Outline each blood parasite and name the species.
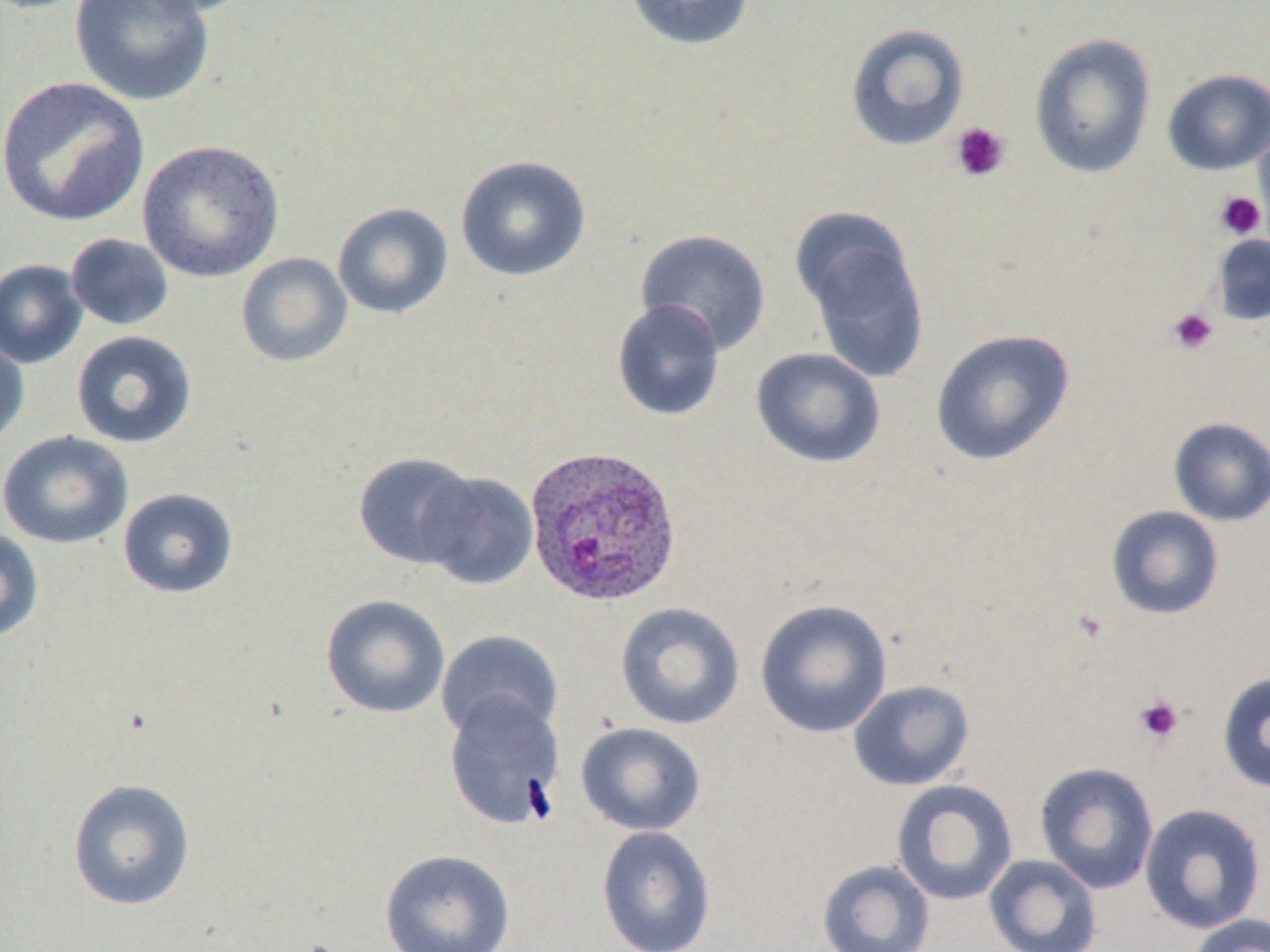
Approximate bounding boxes as (x1,y1)-(x2,y2) corner pairs in pixels.
Plasmodium ovale-infected red blood cells: (523,443)-(682,607).
No Plasmodium falciparum, Plasmodium malariae, Plasmodium vivax, Babesia divergens, or Trypanosoma brucei observed.

Summary:
  - Platelet locations: (950,122)-(1011,183), (1215,191)-(1265,239), (1167,308)-(1219,355), (1072,608)-(1107,645), (1134,695)-(1184,745)
  - Uninfected red blood cell locations: (69,0)-(215,107), (129,0)-(258,17), (624,0)-(756,50), (845,22)-(970,152), (1029,32)-(1156,179), (1162,68)-(1270,175), (0,76)-(150,228), (1253,116)-(1270,247), (137,139)-(285,282), (455,155)-(592,282), (332,202)-(454,319), (792,208)-(931,384), (635,228)-(771,355), (65,233)-(174,331), (1210,233)-(1270,327), (236,253)-(352,367), (0,258)-(89,369), (611,299)-(726,422), (0,328)-(30,452), (929,328)-(1075,467), (71,330)-(197,449), (751,347)-(886,468), (1168,416)-(1270,527), (1,430)-(133,550), (352,452)-(479,569), (417,470)-(538,590), (117,487)-(239,599), (1106,505)-(1224,620), (0,528)-(45,642), (320,594)-(451,719), (755,598)-(893,739), (614,602)-(745,730), (436,630)-(563,741), (1218,672)-(1270,793), (848,679)-(975,791), (443,691)-(566,830), (575,721)-(706,837), (1034,762)-(1160,894), (67,778)-(196,911), (891,780)-(1018,906), (1139,803)-(1267,934), (596,825)-(716,952), (380,848)-(515,952), (984,854)-(1103,952), (817,859)-(935,952), (1188,913)-(1270,952)
  - Slide-level diagnosis: Plasmodium ovale
  - Stain: May-Grünwald-Giemsa
  - Field of view: one of a larger specimen
  - Image size: 1270×952 pixels
  - Preparation: thin blood smear
  - Magnification: 1000x
  - Modality: optical microscopy